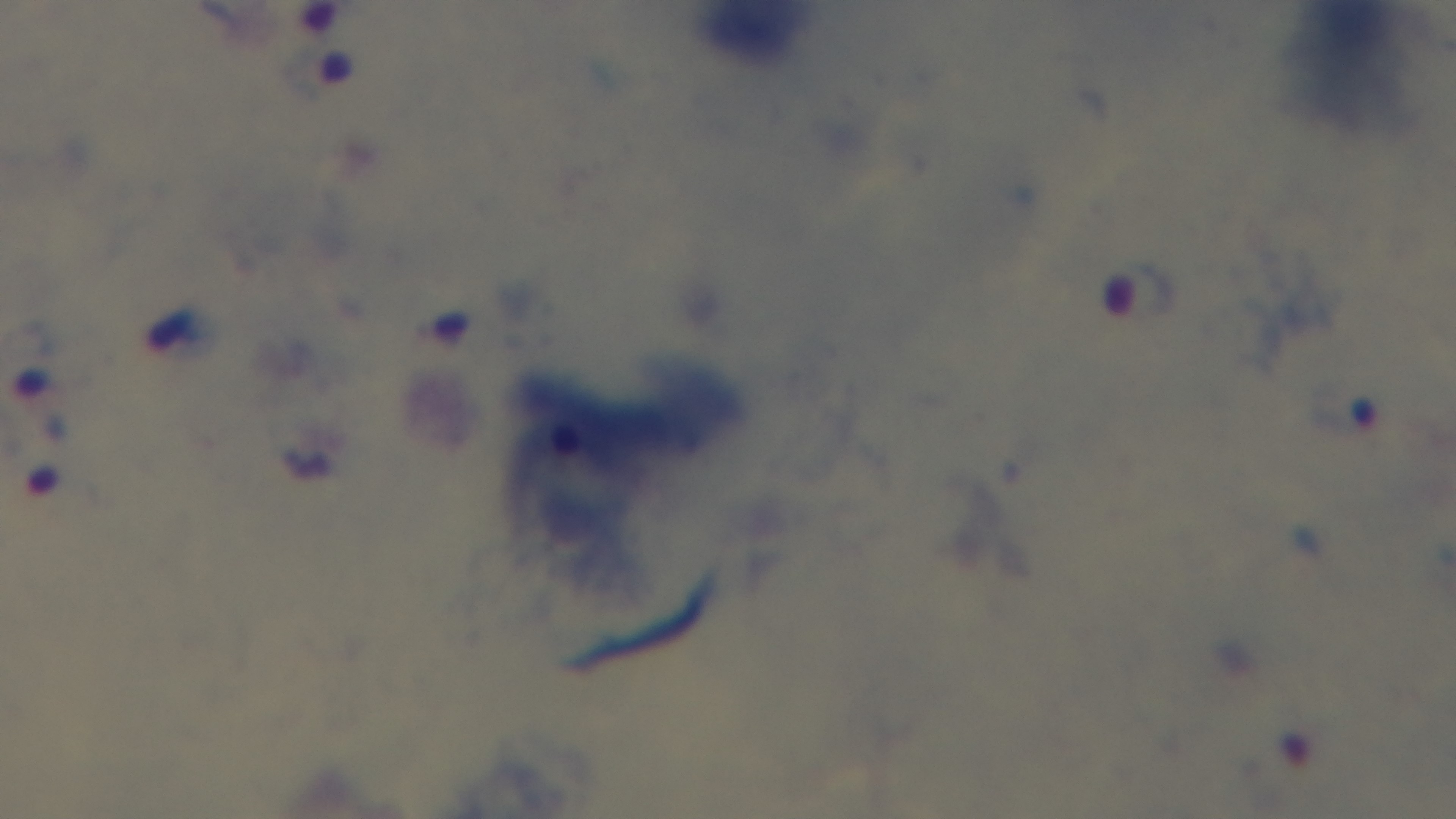
malaria status = positive
objective = 100x oil immersion
modality = light microscopy
stain = Giemsa
capture = mounted 4K digital camera
field of view = single
preparation = thick